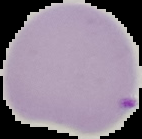
Summary:
  - Preparation: thin blood film
  - Malaria status: parasitized
  - Image type: segmented cell region on a black background
  - Image size: 142×139 pixels